Classify this cell by malaria status.
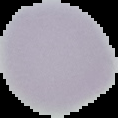
Uninfected.

preparation: thin blood smear
image_type: cell region segmented out of the field of view; surrounding area masked to black
image_size: 118×118 pixels